Describe the morphology of the red blood cells.
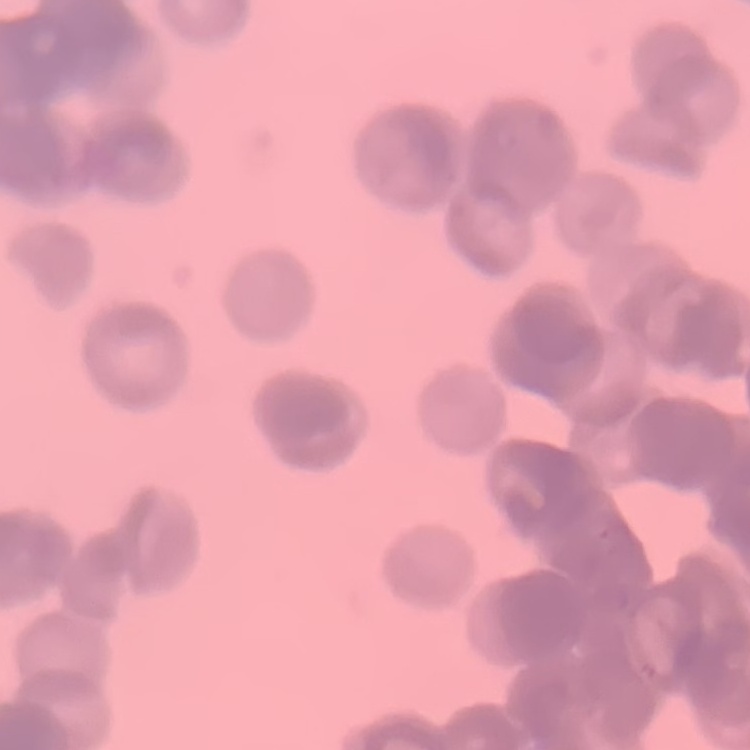

Rouleaux formation.

One tile cut from a larger photomicrograph. Stained with either Field's or Giemsa. Thin peripheral smear.